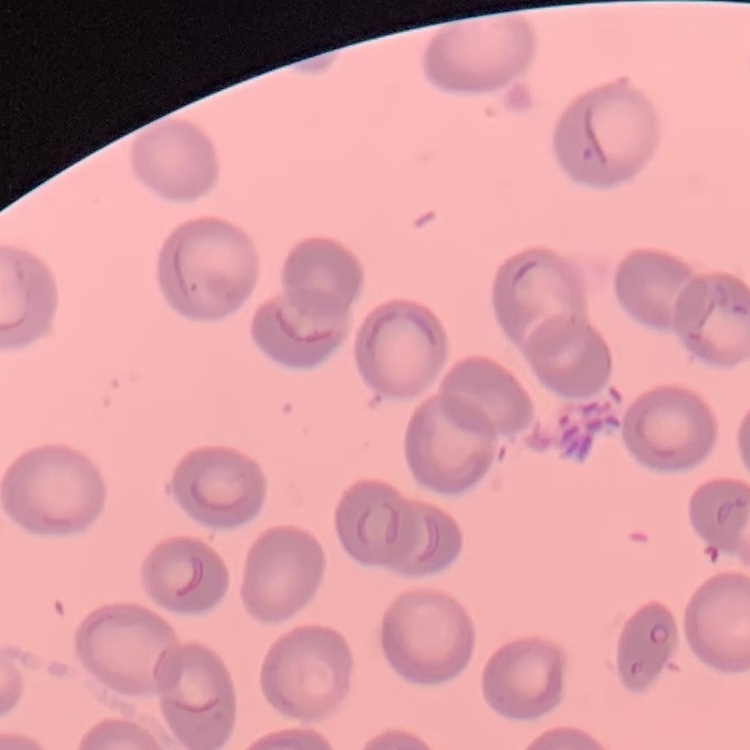
The red blood cells show no rouleaux formation. Stained with either Field's or Giemsa. One tile cut from a larger photomicrograph. Thin blood film.